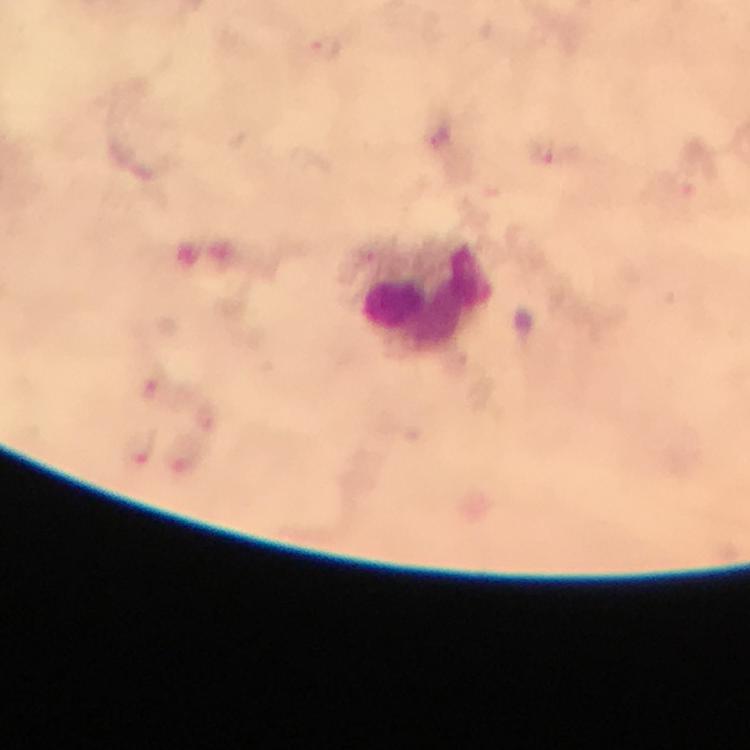

Approximate object centers, in pixels from the top-left corner.
Summary:
  - Plasmodium parasite locations: (x=327, y=48), (x=556, y=154), (x=154, y=384), (x=140, y=449), (x=188, y=459)
  - Leukocyte locations: (x=423, y=297)
  - Capture: smartphone camera through the microscope
  - Preparation: thick blood smear
  - Immersion oil: applied
  - Image size: 750×750 pixels
  - Context: from a malaria diagnostic workup
  - Magnification: 100x
  - Stain: Giemsa
  - Cropped from: one field of view